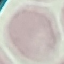
Result: no malaria parasites seen. Giemsa-stained preparation. Thin blood film. Acquired by smartphone through the microscope eyepiece. Automatically extracted cell patch, resized to 64 × 64 pixels.